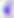 Captured at 400x magnification. Toxoplasma gondii is shown. Micrograph.